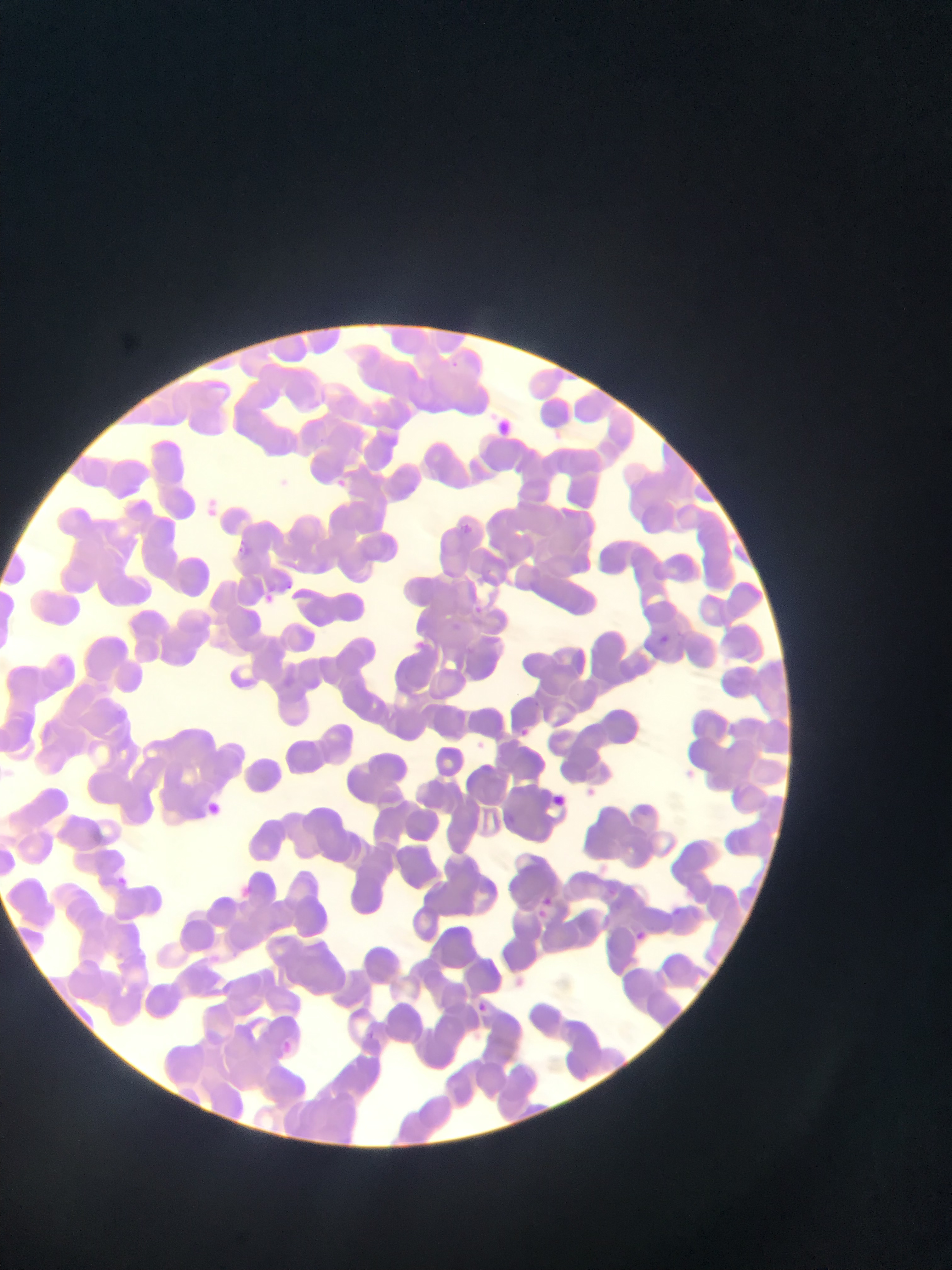

{
  "country": "Ghana",
  "image_size": "952×1270 pixels",
  "preparation": "thin blood smear",
  "capture": "mobile-phone photograph through a microscope",
  "field_of_view": "single",
  "plasmodium_parasite_locations": "approximate bounding boxes as (left, top, right, bottom) in pixels: (489, 410, 518, 432), (337, 474, 354, 497), (461, 519, 488, 538), (234, 544, 246, 561), (257, 578, 282, 605), (473, 594, 490, 611), (658, 630, 672, 647), (398, 634, 428, 654), (514, 717, 532, 739), (550, 789, 577, 811), (199, 793, 219, 820), (109, 867, 138, 886), (233, 880, 252, 897), (536, 893, 562, 930), (667, 901, 686, 918), (632, 925, 665, 956), (472, 993, 496, 1017), (365, 1027, 384, 1045), (281, 1036, 312, 1063)"
}